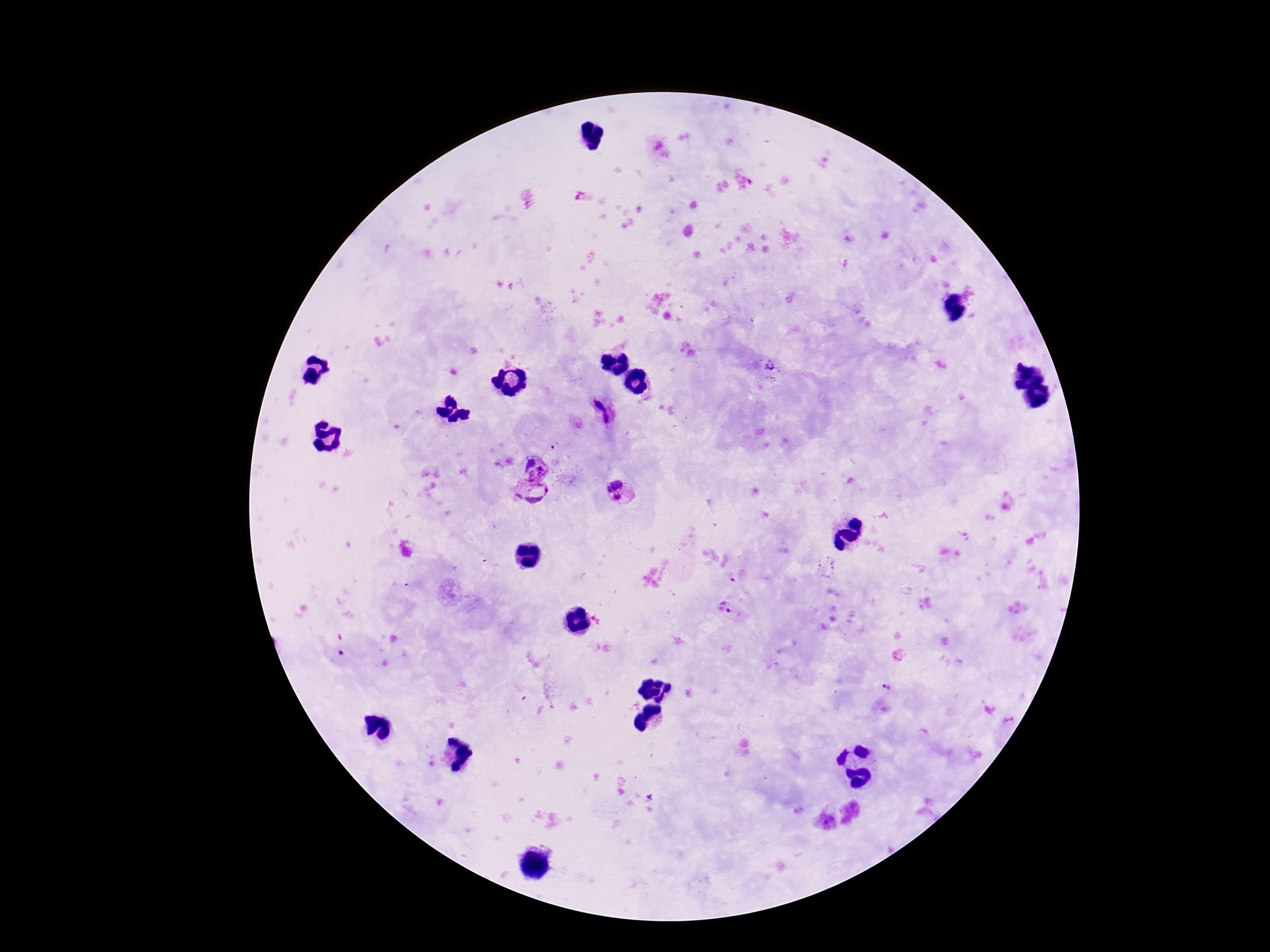
Approximate centers as [x, y] in pixels.
Summary:
  - Plasmodium parasite locations: [772, 367], [602, 410], [534, 466], [612, 483], [533, 493], [617, 497], [826, 567], [726, 609], [888, 686]
  - Field of view: single
  - Patient malaria status: positive
  - Preparation: thick blood smear
  - Capture: smartphone camera through the microscope eyepiece
  - Magnification: 100x
  - Stain: Giemsa
  - Image size: 1270×952 pixels